Describe the morphology of the red blood cells.
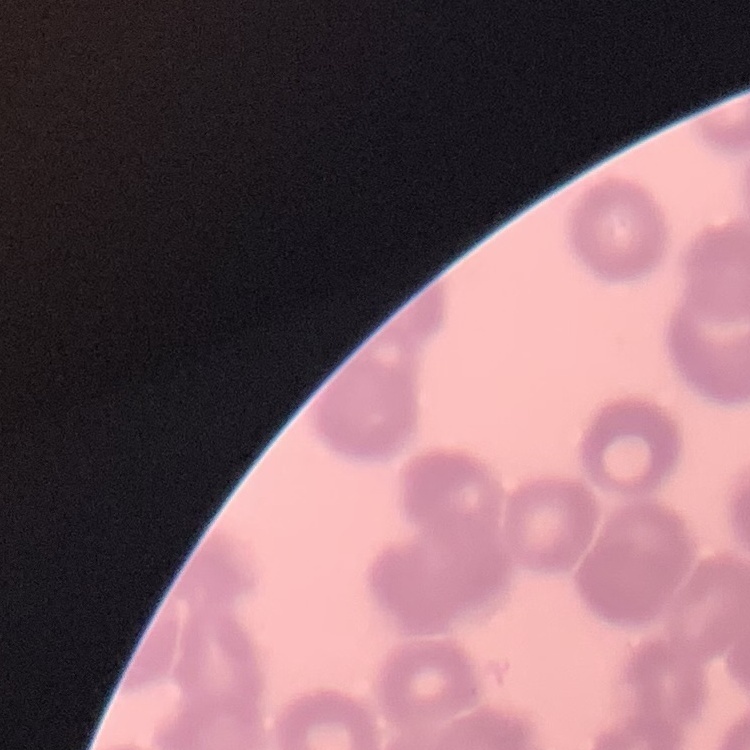

They show rouleaux formation.

Thin peripheral smear. Field's or Giemsa stain. One tile cut from a larger photomicrograph.